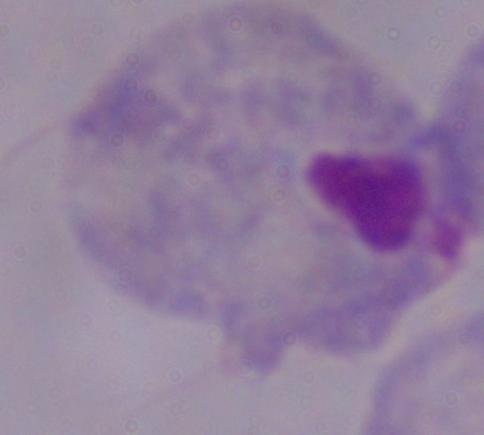
{
  "magnification": "1000x",
  "modality": "micrograph",
  "identification": "trichomonad"
}